Outline each uninfected red blood cell.
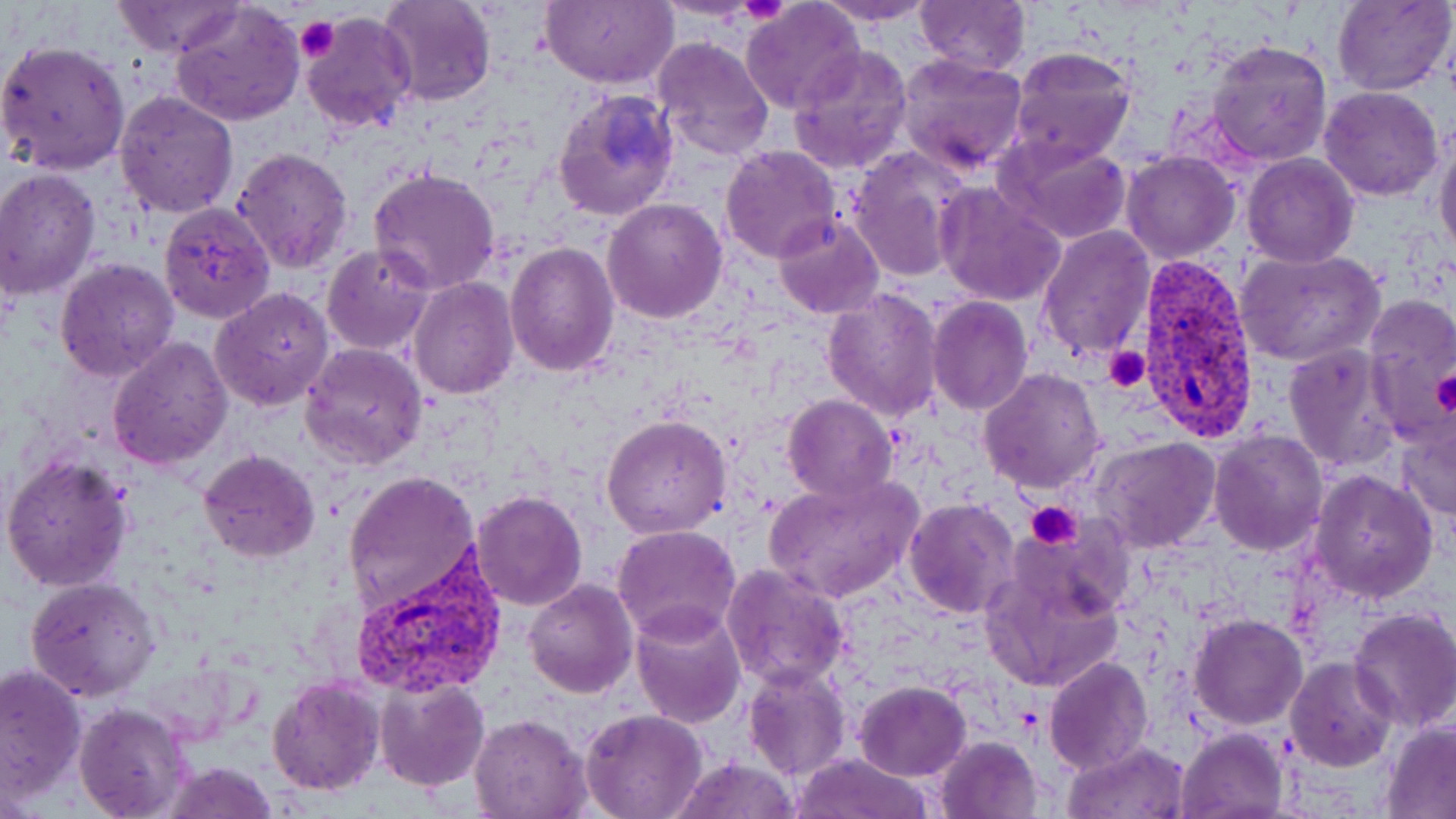
Approximate bounding boxes as (x1,y1)-(x2,y2) corner pairs in pixels.
Uninfected red blood cells: (378,0)-(495,107), (541,0)-(676,88), (913,0)-(1031,77), (1331,0)-(1453,96), (813,1)-(940,26), (108,2)-(245,58), (171,2)-(305,127), (740,3)-(865,116), (298,13)-(415,133), (651,35)-(776,160), (1,39)-(131,174), (1206,39)-(1333,166), (787,44)-(913,175), (1007,45)-(1137,166), (897,52)-(1028,176), (1318,86)-(1445,203), (553,88)-(678,221), (113,90)-(238,218), (1434,128)-(1456,269), (996,136)-(1134,244), (720,145)-(844,263), (848,146)-(973,282), (231,147)-(354,273), (1119,149)-(1240,262), (1242,153)-(1359,268), (0,167)-(101,300), (367,168)-(502,296), (935,183)-(1066,308), (602,197)-(728,322), (159,200)-(276,322), (772,213)-(886,320), (1040,224)-(1153,361), (505,240)-(618,377), (320,245)-(436,354), (1237,248)-(1384,368), (55,258)-(180,383), (408,277)-(519,401), (210,287)-(335,412), (821,287)-(945,421), (1362,295)-(1456,443), (927,296)-(1032,417), (107,336)-(234,468), (299,341)-(428,470), (1284,342)-(1398,472), (978,368)-(1105,494), (783,394)-(897,503), (601,414)-(731,538), (1400,418)-(1456,525), (1208,429)-(1329,557), (1093,436)-(1221,552), (198,451)-(320,564), (0,453)-(134,595), (1308,467)-(1439,602), (341,470)-(480,619), (764,475)-(923,603), (469,490)-(590,611), (903,498)-(1020,619), (613,524)-(742,644), (980,545)-(1126,696), (721,565)-(850,690), (26,575)-(164,702), (522,579)-(637,699), (630,605)-(745,729), (1348,606)-(1456,731), (1190,614)-(1308,729), (1044,655)-(1153,775), (1286,657)-(1397,771), (145,658)-(239,746), (1,661)-(87,806), (744,666)-(850,781), (269,675)-(384,797), (375,676)-(489,790), (853,680)-(971,780), (73,702)-(195,819), (580,710)-(708,819), (469,714)-(592,819), (1382,721)-(1456,816), (1178,727)-(1289,819), (935,735)-(1045,819), (1063,740)-(1190,819), (791,753)-(938,819), (668,755)-(802,818), (161,763)-(279,819).

{
  "slide_level_diagnosis": "Plasmodium vivax",
  "magnification": "1000x",
  "field_of_view": "one of a larger specimen",
  "preparation": "thin blood film",
  "image_size": "1456×819 pixels",
  "stain": "May-Grünwald-Giemsa",
  "platelet_locations": "approximate bounding boxes as (x1,y1)-(x2,y2) corner pairs in pixels: (739,0)-(790,24), (295,18)-(339,62), (1104,347)-(1152,392), (1428,368)-(1456,416), (1025,500)-(1082,550)",
  "modality": "optical microscopy",
  "plasmodium_vivax_infected_red_blood_cell_locations": "approximate bounding boxes as (x1,y1)-(x2,y2) corner pairs in pixels: (1132,256)-(1264,442), (351,553)-(504,698)"
}